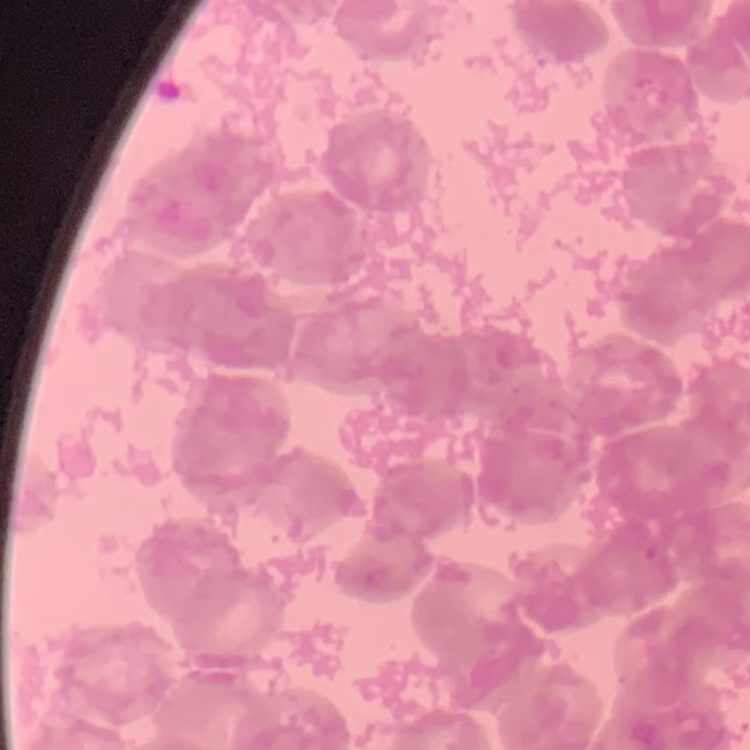

{
  "erythrocyte_morphology": "rouleaux formation",
  "stain": "Field's or Giemsa",
  "image_type": "square crop of a larger photomicrograph",
  "preparation": "thin blood smear"
}